Assess the morphology of the erythrocytes.
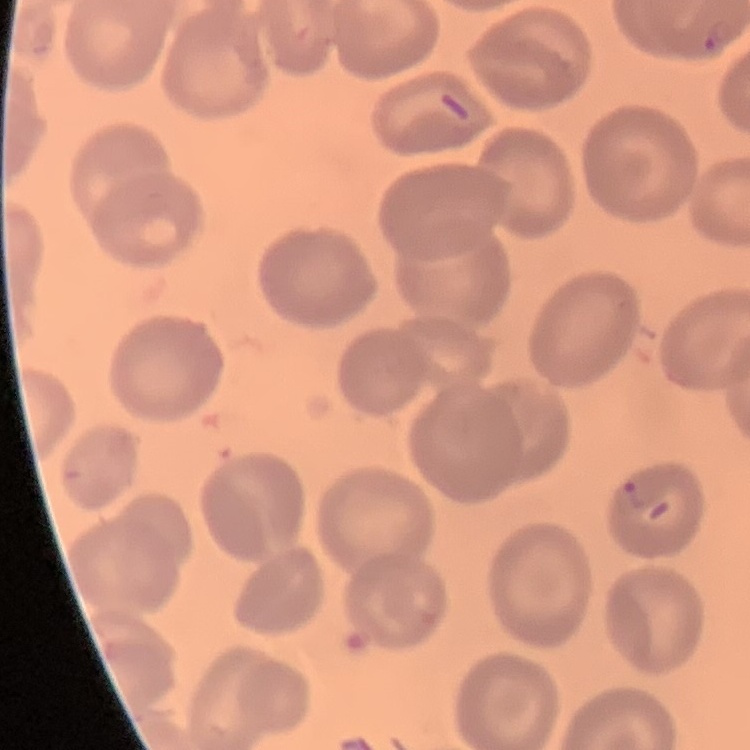

They show no rouleaux formation.

Thin blood smear. Field's or Giemsa stain. Square crop of a larger photomicrograph.